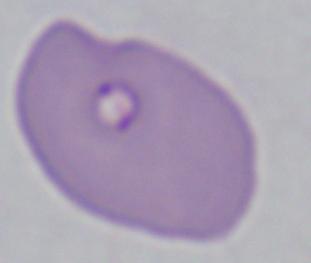
Summary:
  - Modality: micrograph
  - Magnification: 1000x
  - Identification: Babesia